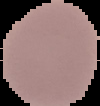
Image is 100×106 pixels. Segmented cell region on a black background. From a thin blood smear. Result: no malaria parasites seen.